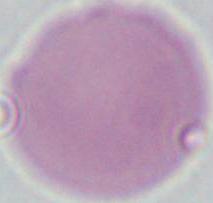 Photomicrograph. Captured at 1000x magnification. An erythrocyte is shown.